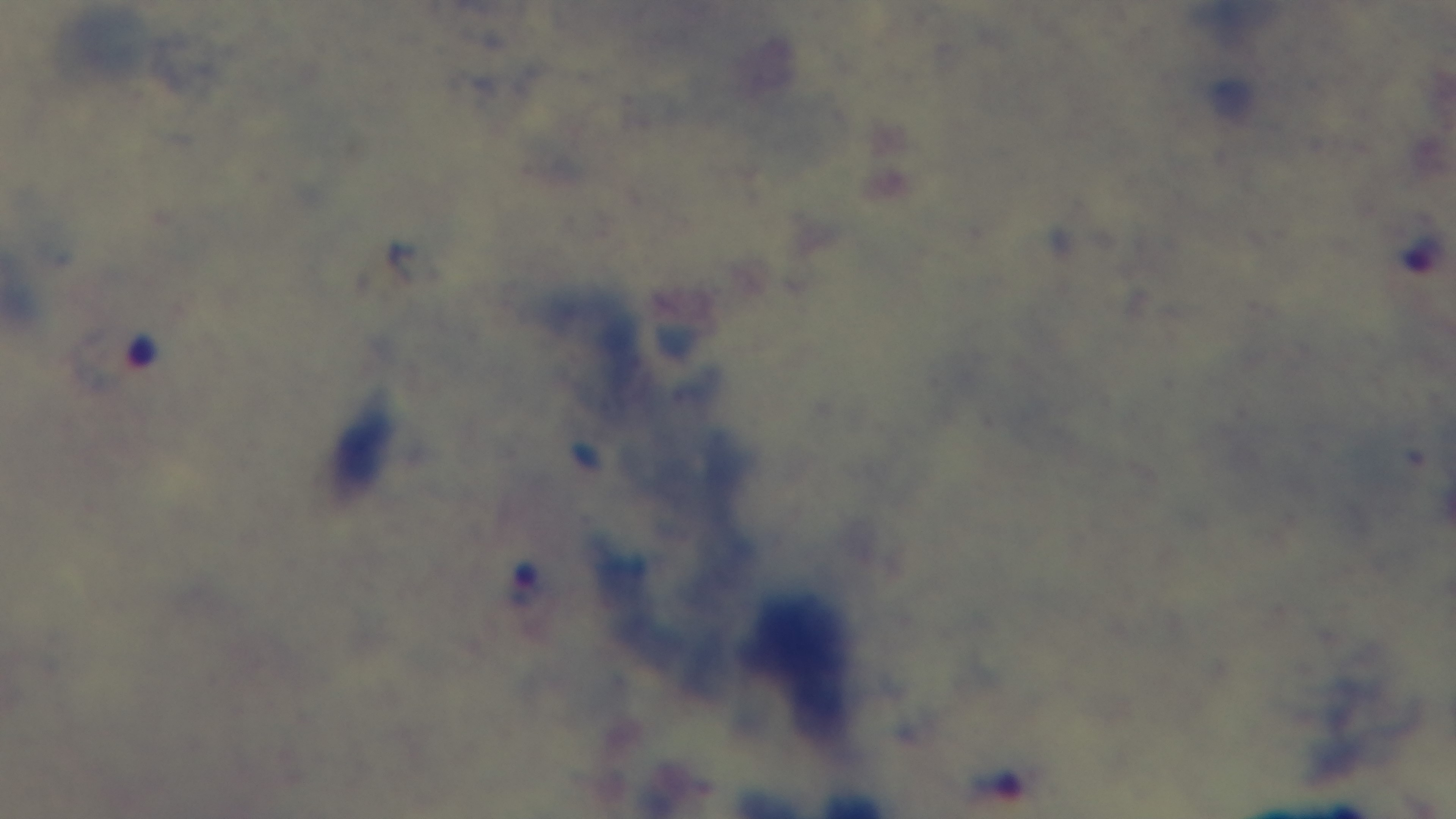 Oil-immersion objective, 100x. Captured with a mounted 4K digital camera. Preparation: thick smear. Light microscopy. Malaria status: positive. Single field of view. Giemsa-stained.